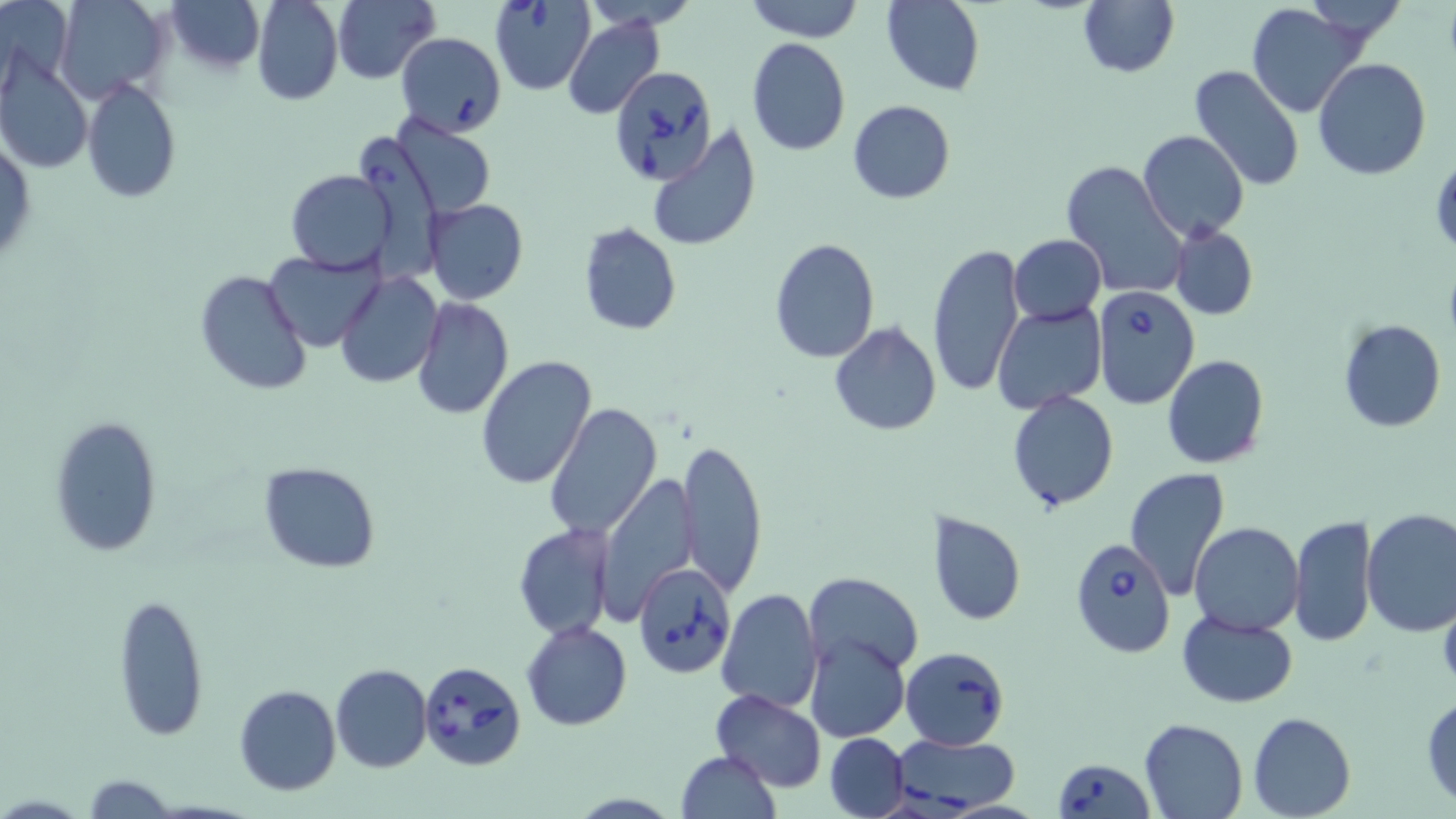

Summary:
  - Coordinate format: approximate bounding boxes as (x1, y1, x2, y2) in pixels
  - Uninfected red blood cell locations: (55, 0, 171, 104), (165, 0, 265, 73), (253, 0, 343, 105), (334, 0, 439, 85), (577, 0, 703, 31), (744, 0, 865, 42), (882, 0, 985, 94), (1078, 0, 1179, 77), (1244, 3, 1365, 118), (563, 15, 665, 120), (746, 37, 851, 156), (1314, 58, 1432, 180), (0, 59, 93, 175), (1189, 64, 1304, 192), (81, 77, 180, 204), (847, 100, 954, 204), (389, 115, 498, 218), (647, 124, 761, 253), (353, 127, 445, 278), (1138, 129, 1249, 243), (1, 137, 35, 266), (1061, 160, 1188, 297), (285, 169, 397, 274), (425, 198, 528, 305), (577, 222, 682, 336), (1169, 224, 1258, 320), (1009, 235, 1105, 322), (769, 237, 880, 364), (927, 243, 1026, 399), (265, 250, 382, 351), (194, 268, 312, 397), (335, 271, 443, 388), (411, 297, 513, 421), (993, 305, 1106, 414), (1338, 320, 1446, 433), (828, 321, 941, 437), (474, 355, 597, 490), (1161, 355, 1270, 470), (1007, 391, 1119, 512), (544, 402, 664, 541), (47, 417, 163, 558), (679, 435, 769, 598), (258, 462, 381, 573), (1124, 467, 1231, 599), (597, 474, 699, 620), (1360, 508, 1456, 635), (928, 510, 1025, 625), (1289, 514, 1377, 648), (1190, 522, 1304, 634), (512, 523, 614, 640), (804, 572, 924, 678), (717, 588, 822, 711), (113, 592, 208, 741), (1176, 609, 1299, 707), (522, 621, 632, 730), (806, 633, 909, 742), (330, 663, 433, 774), (234, 685, 341, 796), (710, 689, 827, 791), (1421, 692, 1456, 807), (1247, 711, 1355, 819), (1139, 717, 1249, 819), (824, 733, 909, 818), (675, 751, 781, 819), (80, 773, 180, 818)
  - Babesia divergens-infected red blood cell locations: (488, 0, 596, 95), (397, 32, 506, 136), (607, 65, 717, 186), (1091, 286, 1200, 410), (1068, 538, 1177, 657), (631, 563, 732, 679), (900, 647, 1009, 750), (416, 657, 526, 770), (888, 734, 1023, 816), (1051, 758, 1153, 818)
  - Slide-level diagnosis: Babesia divergens
  - Stain: May-Grünwald-Giemsa
  - Magnification: 1000x
  - Preparation: thin blood film
  - Image size: 1456×819 pixels
  - Field of view: single
  - Modality: light microscopy